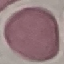

result = no malaria parasites detected
image type = cell patch, automatically extracted from a larger field of view and resized to 64 × 64 pixels
stain = Giemsa
preparation = thin blood film
capture = smartphone through the microscope eyepiece